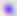

modality = micrograph
identification = Toxoplasma gondii
magnification = 400x